Identify the parasite.
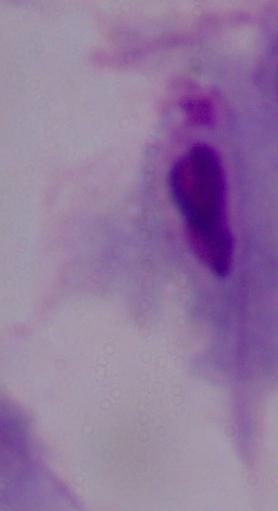

This is a trichomonad.

Photomicrograph. Captured at 1000x magnification.